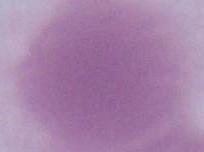
An erythrocyte is seen. 1000x magnification. Micrograph.